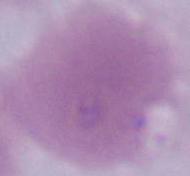

Summary:
  - Identification: erythrocyte
  - Magnification: 1000x
  - Modality: micrograph